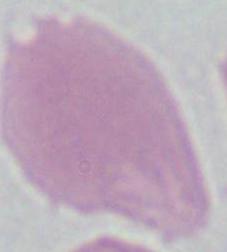

{
  "identification": "erythrocyte",
  "magnification": "1000x",
  "modality": "photomicrograph"
}